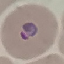
Summary:
  - Malaria status: parasitized
  - Image type: cell patch, automatically extracted from a larger field of view and resized to 64 × 64 pixels
  - Preparation: thin smear
  - Capture: smartphone camera at the microscope eyepiece
  - Stain: Giemsa